State the blood parasite species.
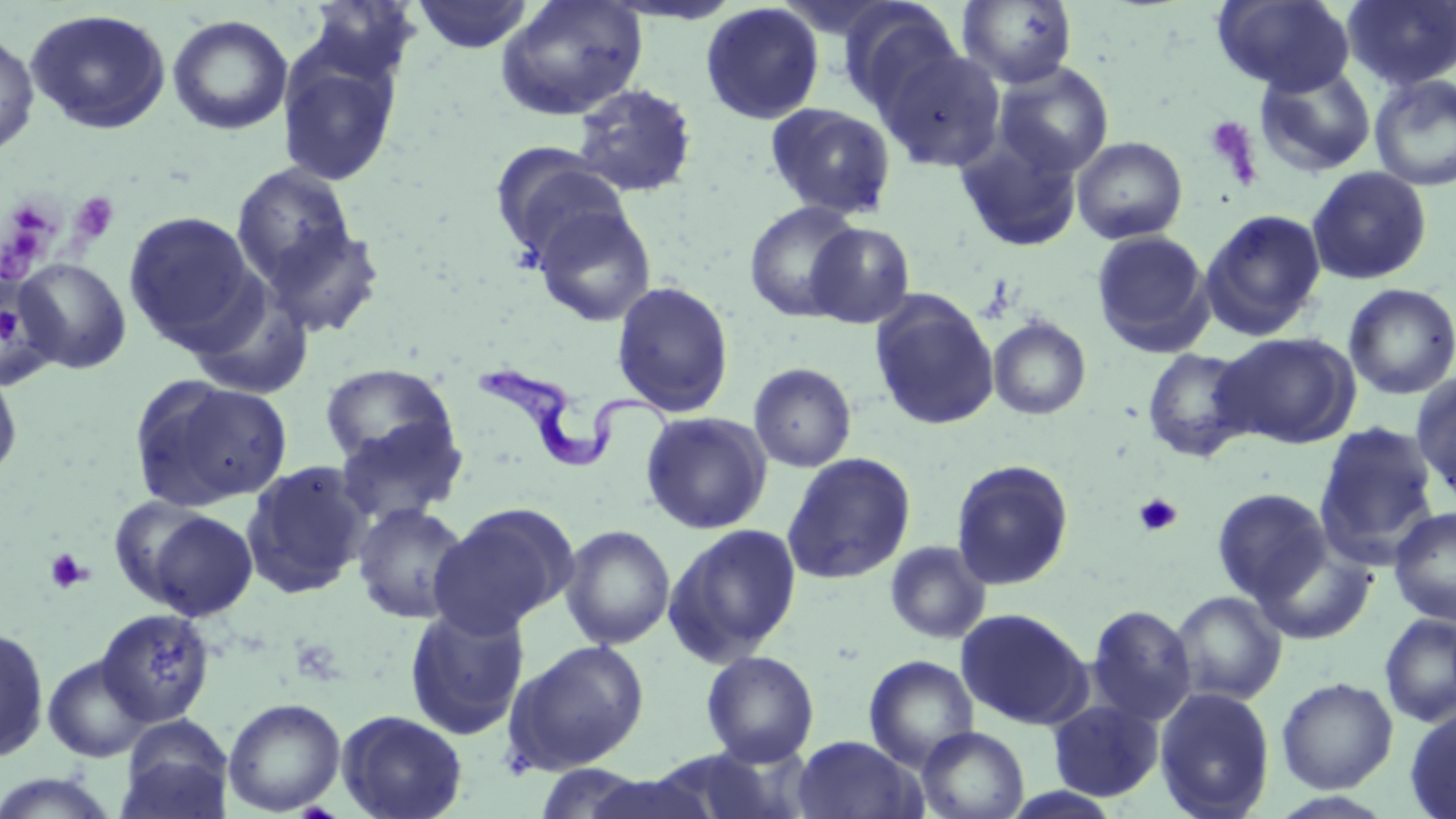

Trypanosoma brucei.

Summary:
  - Coordinate format: approximate bounding boxes as (x1,y1)-(x2,y2) corner pairs in pixels
  - Uninfected red blood cell locations: (411,0)-(536,53), (494,0)-(648,121), (957,0)-(1077,88), (1213,0)-(1355,95), (1343,0)-(1456,90), (700,2)-(825,124), (840,3)-(966,118), (26,8)-(172,134), (167,15)-(293,135), (0,29)-(39,158), (877,45)-(1007,172), (278,50)-(402,187), (993,63)-(1114,178), (1254,63)-(1376,177), (1369,74)-(1456,191), (571,83)-(698,198), (765,102)-(897,219), (955,132)-(1085,253), (1071,136)-(1188,244), (490,144)-(629,265), (231,163)-(359,292), (1306,166)-(1432,285), (744,201)-(864,322), (531,203)-(657,329), (1200,208)-(1327,340), (123,210)-(262,350), (258,219)-(386,338), (805,223)-(915,328), (1091,230)-(1213,356), (14,258)-(132,374), (0,272)-(62,388), (611,281)-(735,417), (1343,283)-(1456,399), (869,292)-(999,430), (988,316)-(1091,420), (1214,332)-(1361,449), (1142,346)-(1256,462), (749,362)-(857,472), (319,363)-(458,471), (0,366)-(23,485), (1411,374)-(1456,498), (130,376)-(293,512), (640,411)-(772,534), (333,416)-(468,527), (1314,421)-(1440,562), (781,452)-(916,585), (951,459)-(1075,590), (241,460)-(372,599), (1211,488)-(1332,605), (106,495)-(216,609), (351,502)-(473,624), (429,503)-(578,637), (1389,506)-(1456,626), (140,508)-(260,620), (664,523)-(803,665), (559,524)-(676,650), (1254,540)-(1375,645), (884,541)-(992,644), (1170,590)-(1287,705), (403,603)-(530,741), (1087,604)-(1197,725), (95,608)-(216,727), (955,608)-(1091,728), (1379,614)-(1456,727), (0,625)-(50,763), (505,640)-(650,774), (701,650)-(820,765), (42,654)-(155,763), (864,654)-(978,769), (1276,677)-(1398,794), (1154,688)-(1275,819), (223,697)-(346,815), (1047,699)-(1164,802), (1405,706)-(1456,819), (335,709)-(468,819), (117,716)-(235,819), (917,727)-(1029,819), (792,735)-(925,819), (533,763)-(653,819), (0,771)-(123,818), (581,771)-(716,819)
  - Trypanosoma brucei locations: (473,363)-(682,467)
  - Platelet locations: (1203,116)-(1260,182), (70,192)-(119,245), (10,209)-(57,240), (10,227)-(42,255), (1133,493)-(1182,536), (44,548)-(92,593)
  - Magnification: 1000x
  - Field of view: single
  - Modality: light microscopy
  - Image size: 1456×819 pixels
  - Preparation: thin blood smear
  - Stain: May-Grünwald-Giemsa